Assess the morphology of the red blood cells.
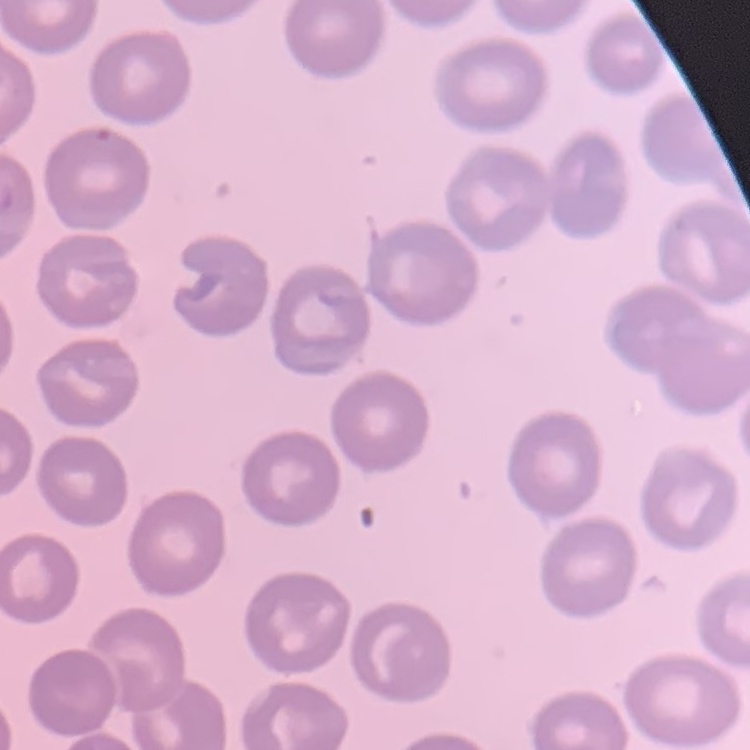
They show no rouleaux formation.

stain = Field's or Giemsa
preparation = thin blood smear
image type = one tile cut from a larger photomicrograph